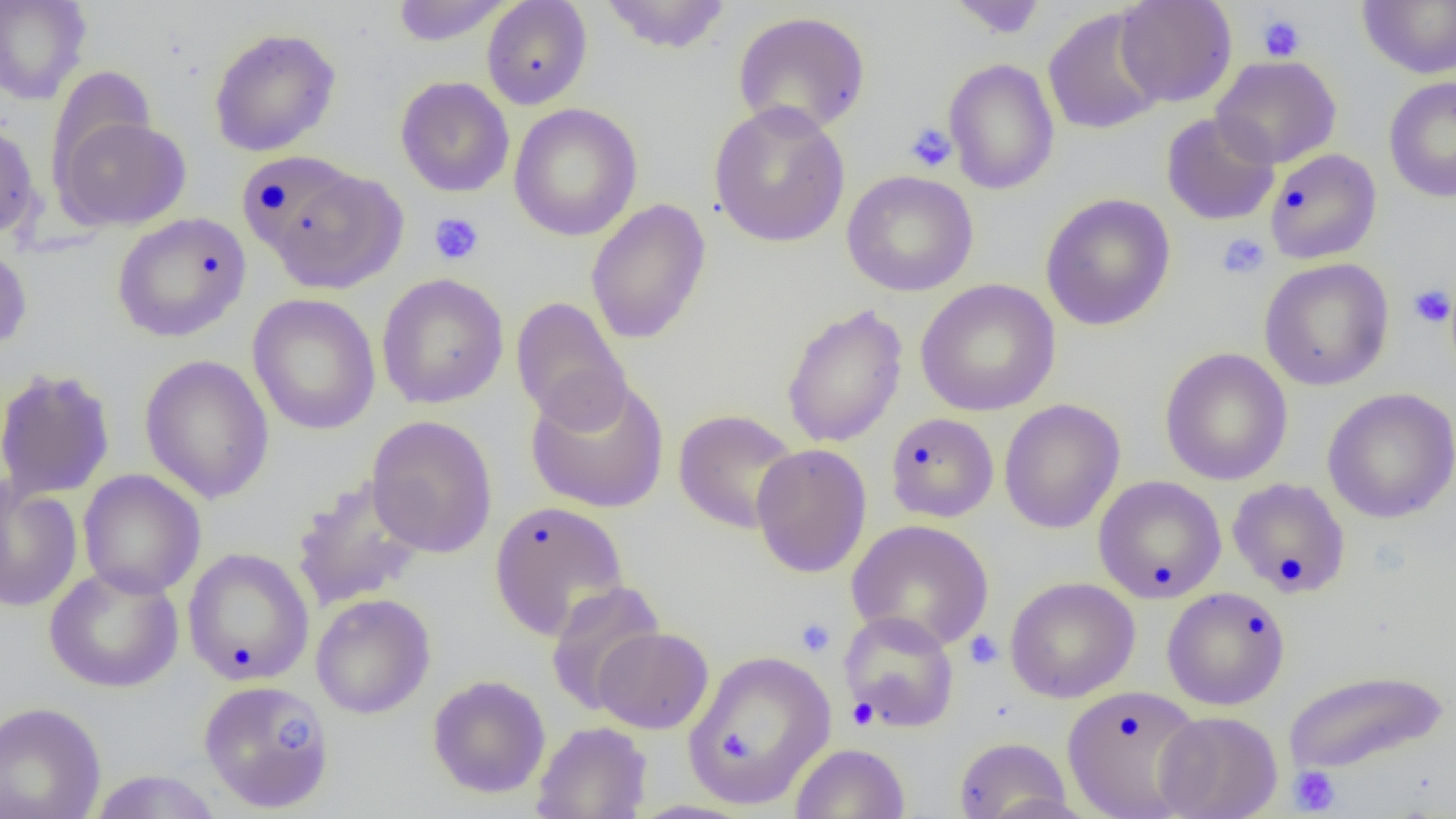
slide_level_diagnosis: negative for blood parasites
uninfected_red_blood_cell_locations: 'approximate bounding boxes as named x1/y1/x2/y2 corners in pixels: (x1=0, y1=0, x2=91, y2=105), (x1=599, y1=0, x2=732, y2=55), (x1=946, y1=0, x2=1050, y2=39), (x1=1115, y1=0, x2=1237, y2=108), (x1=1358, y1=0, x2=1456, y2=79), (x1=390, y1=1, x2=513, y2=46), (x1=481, y1=1, x2=593, y2=110), (x1=1043, y1=8, x2=1166, y2=135), (x1=732, y1=10, x2=871, y2=137), (x1=208, y1=27, x2=342, y2=157), (x1=1211, y1=55, x2=1342, y2=169), (x1=942, y1=58, x2=1060, y2=195), (x1=45, y1=67, x2=158, y2=181), (x1=395, y1=76, x2=515, y2=197), (x1=1384, y1=76, x2=1456, y2=202), (x1=708, y1=101, x2=851, y2=248), (x1=508, y1=103, x2=642, y2=242), (x1=1161, y1=112, x2=1281, y2=226), (x1=53, y1=113, x2=192, y2=231), (x1=0, y1=120, x2=40, y2=241), (x1=1264, y1=148, x2=1381, y2=264), (x1=251, y1=163, x2=407, y2=294), (x1=841, y1=170, x2=979, y2=296), (x1=1040, y1=193, x2=1176, y2=330), (x1=586, y1=199, x2=712, y2=344), (x1=111, y1=212, x2=251, y2=342), (x1=0, y1=238, x2=33, y2=354), (x1=1259, y1=258, x2=1394, y2=391), (x1=376, y1=273, x2=509, y2=410), (x1=915, y1=279, x2=1060, y2=416), (x1=247, y1=293, x2=381, y2=436), (x1=511, y1=297, x2=631, y2=430), (x1=781, y1=303, x2=908, y2=448), (x1=1159, y1=347, x2=1293, y2=485), (x1=138, y1=354, x2=275, y2=504), (x1=0, y1=367, x2=116, y2=501), (x1=524, y1=373, x2=670, y2=513), (x1=1323, y1=387, x2=1455, y2=524), (x1=999, y1=398, x2=1125, y2=534), (x1=673, y1=409, x2=801, y2=533), (x1=885, y1=412, x2=999, y2=523), (x1=366, y1=414, x2=498, y2=558), (x1=751, y1=443, x2=872, y2=578), (x1=77, y1=469, x2=206, y2=599), (x1=290, y1=474, x2=428, y2=610), (x1=1093, y1=475, x2=1226, y2=603), (x1=1226, y1=477, x2=1351, y2=598), (x1=0, y1=480, x2=83, y2=613), (x1=488, y1=500, x2=630, y2=641), (x1=846, y1=518, x2=994, y2=651), (x1=182, y1=547, x2=315, y2=687), (x1=44, y1=565, x2=184, y2=693), (x1=1005, y1=577, x2=1140, y2=703), (x1=544, y1=580, x2=666, y2=717), (x1=1163, y1=587, x2=1290, y2=710), (x1=310, y1=593, x2=436, y2=719), (x1=839, y1=611, x2=960, y2=732), (x1=592, y1=626, x2=714, y2=734), (x1=680, y1=649, x2=837, y2=810), (x1=1283, y1=669, x2=1448, y2=775), (x1=427, y1=674, x2=551, y2=798), (x1=197, y1=679, x2=336, y2=813), (x1=1061, y1=684, x2=1205, y2=819), (x1=0, y1=701, x2=107, y2=819), (x1=1155, y1=710, x2=1283, y2=819), (x1=531, y1=721, x2=652, y2=818), (x1=953, y1=736, x2=1073, y2=819), (x1=790, y1=742, x2=910, y2=819), (x1=86, y1=769, x2=224, y2=818)'
magnification: 1000x
modality: optical microscopy
platelet_locations: 'approximate bounding boxes as named x1/y1/x2/y2 corners in pixels: (x1=1257, y1=14, x2=1306, y2=62), (x1=904, y1=122, x2=957, y2=173), (x1=428, y1=212, x2=484, y2=266), (x1=1216, y1=232, x2=1270, y2=280), (x1=1408, y1=284, x2=1454, y2=329), (x1=794, y1=616, x2=836, y2=658), (x1=964, y1=630, x2=1003, y2=669), (x1=846, y1=698, x2=878, y2=729), (x1=259, y1=715, x2=316, y2=770), (x1=721, y1=734, x2=753, y2=755), (x1=1289, y1=766, x2=1340, y2=815)'
image_size: 1456×819 pixels
preparation: thin blood film
field_of_view: one of a larger specimen